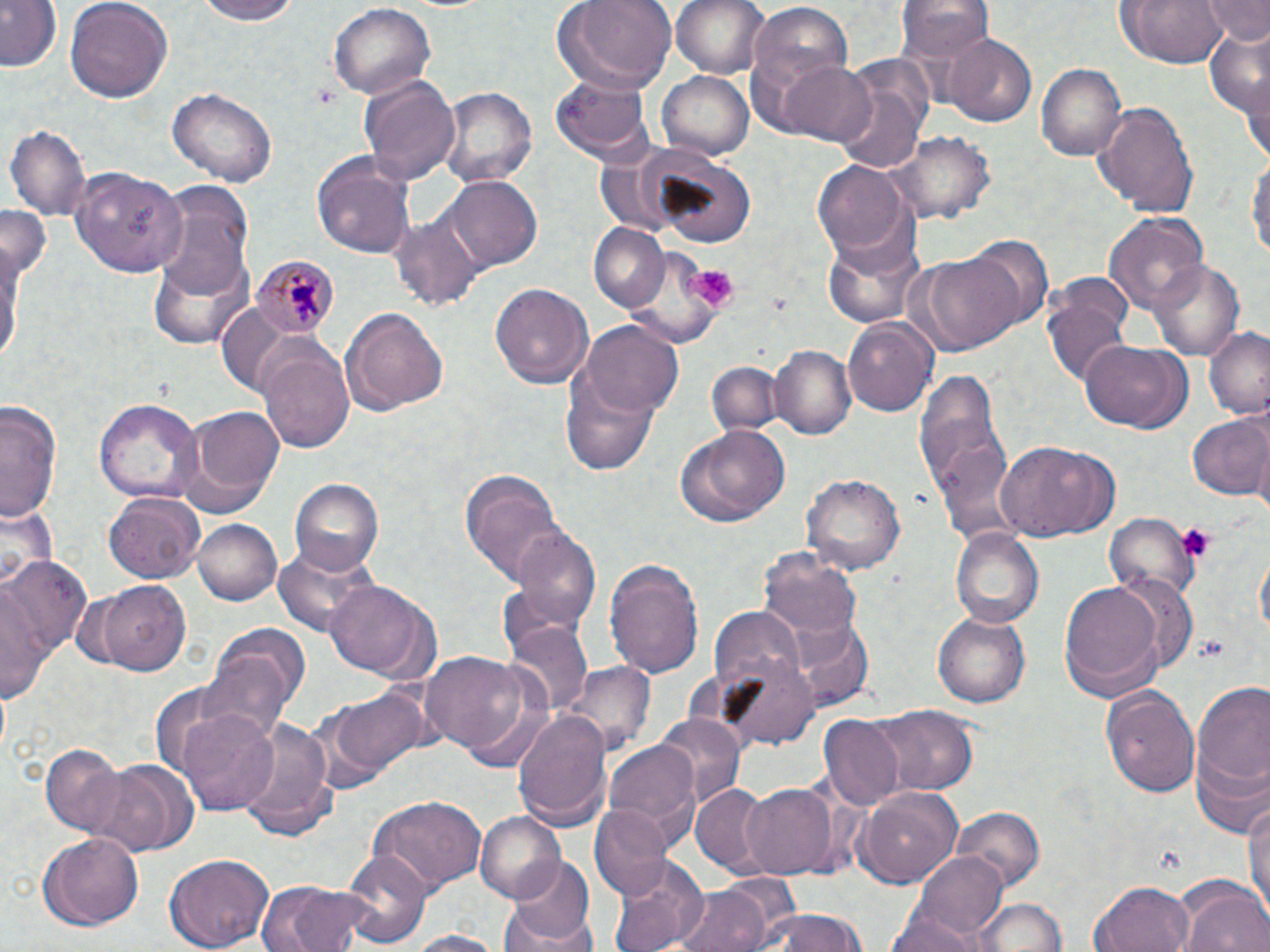
slide-level diagnosis = Plasmodium malariae
magnification = 1000x
image size = 1270×952 pixels
uninfected red blood cell locations = approximate bounding boxes as named x1/y1/x2/y2 corners in pixels: (x1=0, y1=0, x2=62, y2=72), (x1=63, y1=0, x2=173, y2=105), (x1=188, y1=0, x2=309, y2=25), (x1=552, y1=0, x2=677, y2=91), (x1=672, y1=0, x2=769, y2=80), (x1=1115, y1=0, x2=1230, y2=68), (x1=1199, y1=0, x2=1270, y2=45), (x1=898, y1=1, x2=992, y2=64), (x1=326, y1=3, x2=437, y2=102), (x1=747, y1=4, x2=855, y2=111), (x1=1200, y1=25, x2=1270, y2=122), (x1=944, y1=34, x2=1036, y2=126), (x1=1238, y1=53, x2=1270, y2=167), (x1=780, y1=61, x2=878, y2=147), (x1=1036, y1=64, x2=1127, y2=161), (x1=657, y1=71, x2=752, y2=159), (x1=834, y1=72, x2=929, y2=178), (x1=549, y1=75, x2=652, y2=159), (x1=359, y1=76, x2=462, y2=186), (x1=440, y1=85, x2=536, y2=187), (x1=168, y1=88, x2=278, y2=187), (x1=1092, y1=99, x2=1201, y2=216), (x1=6, y1=125, x2=90, y2=220), (x1=893, y1=132, x2=993, y2=224), (x1=1247, y1=150, x2=1269, y2=265), (x1=636, y1=152, x2=759, y2=247), (x1=312, y1=154, x2=416, y2=257), (x1=813, y1=159, x2=912, y2=259), (x1=67, y1=165, x2=186, y2=277), (x1=445, y1=178, x2=541, y2=271), (x1=149, y1=182, x2=254, y2=317), (x1=0, y1=202, x2=51, y2=285), (x1=390, y1=210, x2=485, y2=315), (x1=1103, y1=210, x2=1209, y2=315), (x1=588, y1=223, x2=670, y2=311), (x1=820, y1=229, x2=927, y2=333), (x1=965, y1=234, x2=1053, y2=333), (x1=0, y1=236, x2=28, y2=367), (x1=901, y1=253, x2=1026, y2=354), (x1=1150, y1=257, x2=1245, y2=364), (x1=1044, y1=281, x2=1134, y2=390), (x1=490, y1=282, x2=593, y2=390), (x1=343, y1=307, x2=449, y2=416), (x1=843, y1=315, x2=939, y2=416), (x1=581, y1=322, x2=683, y2=417), (x1=1203, y1=325, x2=1270, y2=419), (x1=1081, y1=340, x2=1193, y2=434), (x1=772, y1=345, x2=855, y2=439), (x1=260, y1=346, x2=356, y2=454), (x1=706, y1=360, x2=781, y2=440), (x1=560, y1=365, x2=660, y2=477), (x1=915, y1=369, x2=1012, y2=535), (x1=95, y1=398, x2=202, y2=502), (x1=1, y1=400, x2=63, y2=524), (x1=173, y1=406, x2=288, y2=520), (x1=1186, y1=411, x2=1270, y2=501), (x1=676, y1=423, x2=788, y2=527), (x1=998, y1=440, x2=1118, y2=539), (x1=459, y1=468, x2=570, y2=586), (x1=801, y1=471, x2=905, y2=572), (x1=289, y1=479, x2=385, y2=576), (x1=103, y1=493, x2=203, y2=584), (x1=1108, y1=515, x2=1195, y2=595), (x1=193, y1=517, x2=282, y2=606), (x1=512, y1=527, x2=600, y2=631), (x1=951, y1=528, x2=1042, y2=627), (x1=273, y1=541, x2=382, y2=638), (x1=760, y1=547, x2=862, y2=638), (x1=1, y1=554, x2=93, y2=685), (x1=605, y1=557, x2=706, y2=678), (x1=5, y1=575, x2=53, y2=709), (x1=91, y1=578, x2=192, y2=673), (x1=324, y1=579, x2=436, y2=680), (x1=1057, y1=579, x2=1168, y2=703), (x1=709, y1=606, x2=806, y2=693), (x1=933, y1=611, x2=1032, y2=707), (x1=781, y1=616, x2=875, y2=709), (x1=202, y1=623, x2=308, y2=736), (x1=505, y1=623, x2=591, y2=717), (x1=419, y1=650, x2=543, y2=766), (x1=712, y1=655, x2=820, y2=750), (x1=564, y1=663, x2=654, y2=758), (x1=1188, y1=680, x2=1270, y2=823), (x1=310, y1=683, x2=435, y2=792), (x1=1102, y1=683, x2=1200, y2=801), (x1=875, y1=703, x2=977, y2=795), (x1=175, y1=704, x2=282, y2=815), (x1=512, y1=706, x2=612, y2=830), (x1=652, y1=711, x2=745, y2=807), (x1=819, y1=714, x2=907, y2=809), (x1=238, y1=716, x2=341, y2=838), (x1=605, y1=741, x2=702, y2=847), (x1=40, y1=745, x2=127, y2=836), (x1=94, y1=759, x2=199, y2=855), (x1=740, y1=782, x2=840, y2=880), (x1=690, y1=783, x2=775, y2=877), (x1=857, y1=784, x2=964, y2=890), (x1=1243, y1=789, x2=1270, y2=920), (x1=366, y1=796, x2=485, y2=892), (x1=589, y1=806, x2=673, y2=900), (x1=951, y1=807, x2=1044, y2=887), (x1=474, y1=810, x2=564, y2=902), (x1=39, y1=830, x2=145, y2=929), (x1=342, y1=850, x2=430, y2=947), (x1=912, y1=851, x2=1009, y2=943), (x1=164, y1=853, x2=276, y2=951), (x1=504, y1=855, x2=594, y2=946), (x1=609, y1=858, x2=706, y2=952), (x1=254, y1=879, x2=378, y2=952), (x1=1090, y1=880, x2=1195, y2=952), (x1=1176, y1=881, x2=1270, y2=952), (x1=672, y1=884, x2=772, y2=952), (x1=969, y1=897, x2=1068, y2=951), (x1=501, y1=905, x2=594, y2=952), (x1=756, y1=909, x2=869, y2=952), (x1=885, y1=910, x2=984, y2=952), (x1=398, y1=930, x2=511, y2=952)
platelet locations = approximate bounding boxes as named x1/y1/x2/y2 corners in pixels: (x1=310, y1=84, x2=342, y2=109), (x1=687, y1=269, x2=742, y2=309), (x1=1174, y1=523, x2=1218, y2=563)
field of view = single
Plasmodium malariae-infected red blood cell locations = approximate bounding boxes as named x1/y1/x2/y2 corners in pixels: (x1=251, y1=257, x2=339, y2=341)
stain = May-Grünwald-Giemsa
modality = light microscopy
preparation = thin blood film